Classify this cell by malaria status.
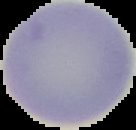

It is uninfected.

From a thin blood smear. The area outside the segmented cell region is set to black. Image is 136×130 pixels.